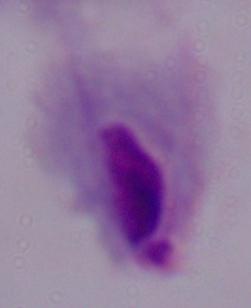

Summary:
  - Modality: photomicrograph
  - Identification: trichomonad
  - Magnification: 1000x